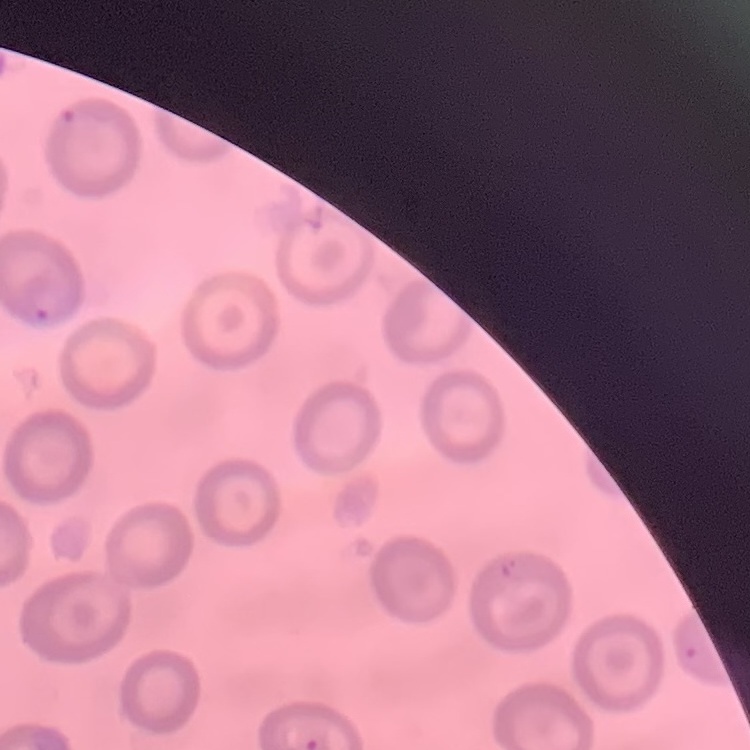

red blood cell morphology = no rouleaux formation
stain = Field's or Giemsa
image type = one tile cut from a larger photomicrograph
preparation = thin blood film